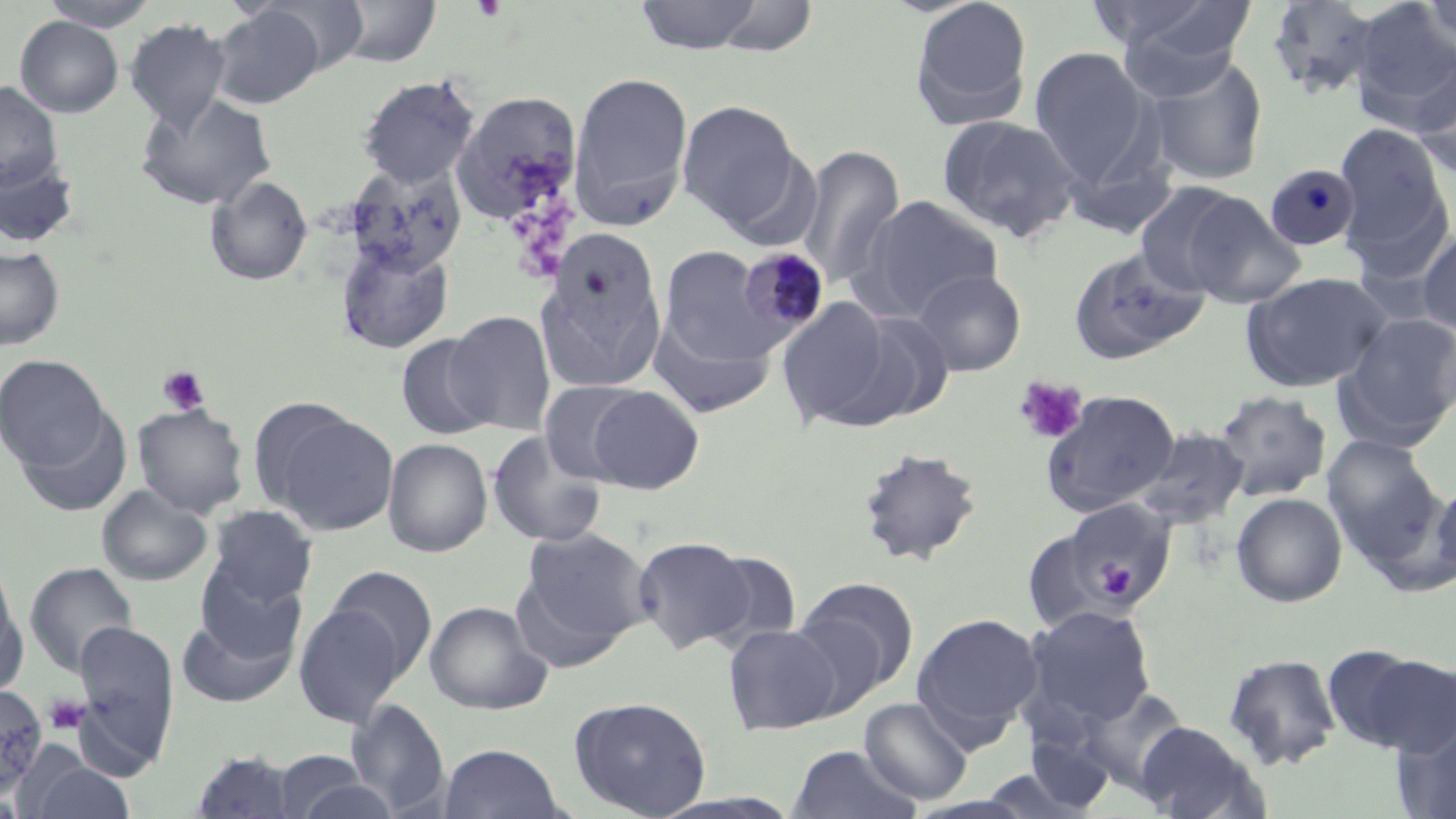 Approximate bounding boxes as [x1, y1, x2, y2] in pixels. Uninfected red blood cell locations: [39, 0, 161, 31], [262, 0, 370, 76], [333, 0, 442, 67], [633, 0, 766, 54], [908, 0, 1034, 130], [1104, 0, 1257, 96], [1264, 0, 1386, 99], [1416, 0, 1456, 61], [704, 1, 821, 57], [1348, 4, 1456, 128], [212, 5, 326, 109], [15, 16, 123, 118], [126, 19, 230, 131], [1029, 47, 1152, 188], [1146, 57, 1269, 186], [1412, 65, 1456, 180], [568, 71, 693, 229], [358, 74, 480, 189], [0, 81, 63, 193], [135, 91, 276, 211], [451, 91, 583, 226], [676, 100, 804, 233], [936, 114, 1082, 243], [1334, 122, 1451, 255], [794, 144, 905, 290], [0, 154, 80, 248], [343, 162, 467, 276], [206, 175, 312, 286], [1134, 182, 1253, 297], [1342, 184, 1454, 287], [1179, 191, 1306, 308], [856, 195, 1003, 320], [1417, 226, 1456, 336], [537, 239, 668, 387], [336, 241, 453, 353], [1068, 245, 1210, 366], [0, 246, 65, 350], [659, 247, 775, 368], [911, 269, 1026, 376], [1239, 271, 1391, 392], [777, 298, 896, 428], [839, 307, 955, 426], [445, 310, 556, 434], [1337, 312, 1456, 446], [652, 313, 776, 420], [396, 334, 496, 439], [0, 354, 109, 471], [539, 380, 646, 485], [585, 385, 704, 493], [1040, 389, 1180, 516], [1213, 390, 1331, 501], [132, 403, 249, 517], [18, 407, 132, 518], [267, 408, 399, 535], [1132, 429, 1248, 529], [487, 431, 608, 549], [1322, 434, 1445, 567], [383, 438, 493, 557], [857, 448, 983, 566], [1431, 473, 1456, 585], [97, 484, 212, 586], [1231, 492, 1347, 607], [1061, 498, 1177, 611], [207, 505, 318, 607], [517, 526, 652, 657], [1022, 527, 1123, 632], [632, 536, 763, 655], [694, 549, 804, 652], [195, 560, 307, 664], [25, 562, 138, 677], [324, 565, 438, 683], [793, 577, 917, 701], [0, 583, 26, 698], [424, 600, 552, 714], [294, 602, 408, 728], [1023, 605, 1157, 730], [177, 611, 298, 707], [911, 611, 1043, 744], [72, 620, 180, 770], [723, 623, 841, 734], [1323, 646, 1451, 754], [1222, 654, 1342, 770], [0, 685, 47, 796], [1077, 686, 1193, 794], [569, 695, 712, 818], [859, 697, 973, 805], [348, 698, 450, 815], [1134, 720, 1268, 819], [1394, 721, 1456, 819], [1022, 728, 1116, 813], [438, 744, 567, 818], [787, 744, 922, 819], [190, 751, 302, 818], [271, 751, 385, 817], [27, 761, 135, 819]. Platelet locations: [157, 366, 210, 416], [1013, 375, 1088, 444], [1095, 561, 1139, 601], [45, 695, 89, 735]. Plasmodium malariae-infected red blood cell locations: [1265, 164, 1360, 251], [736, 246, 830, 342]. Slide-level diagnosis: Plasmodium malariae. 1000x magnification. Single field of view. Optical microscopy. May-Grünwald-Giemsa-stained preparation. Thin blood film. Image is 1456×819 pixels.